Identify the preparation type.
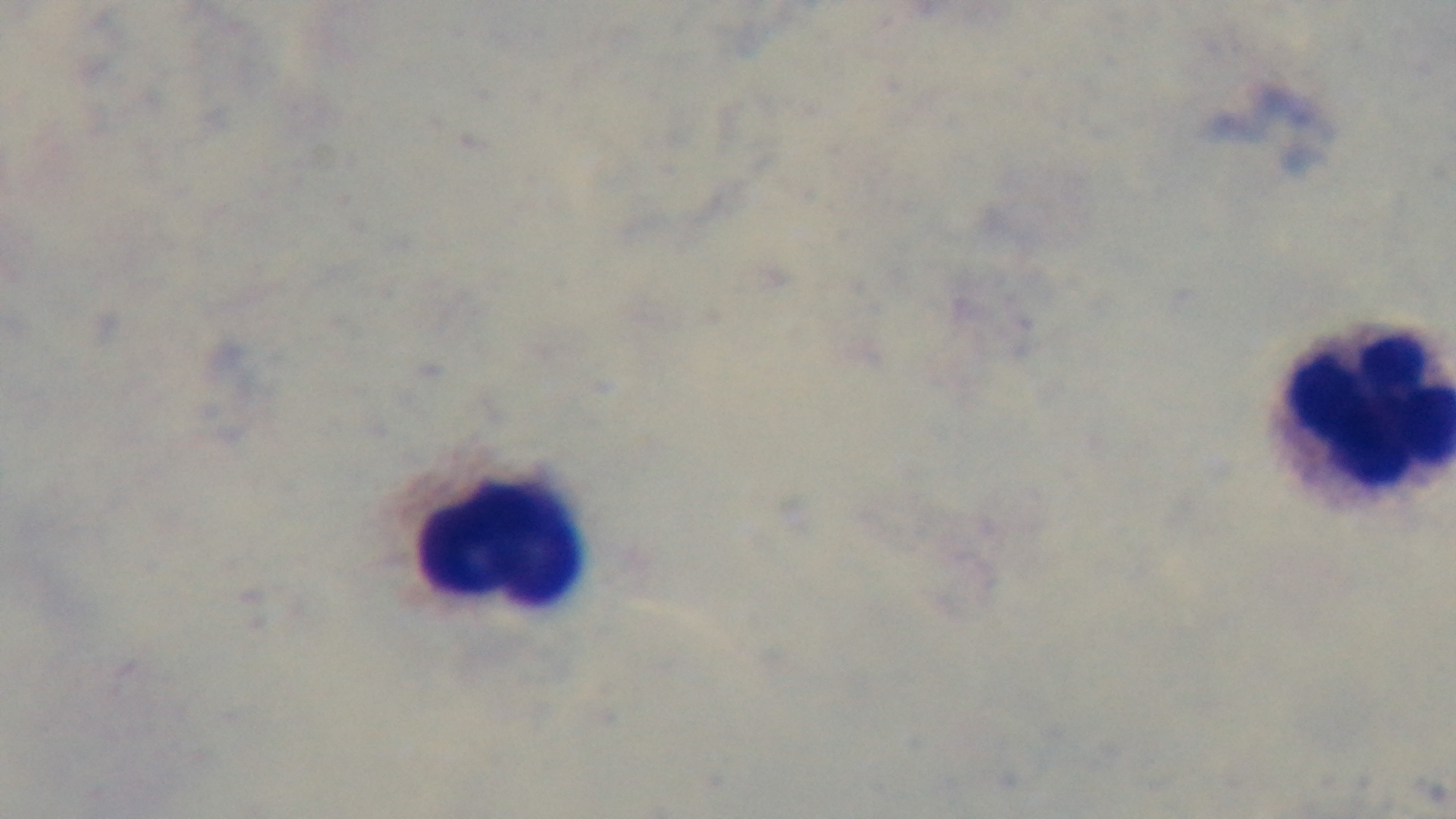
It is a thick blood film.

Summary:
  - Modality: light microscopy
  - Stain: Giemsa
  - Objective: 100x oil immersion
  - Field of view: single
  - Capture: mounted 4K digital camera
  - Malaria status: negative